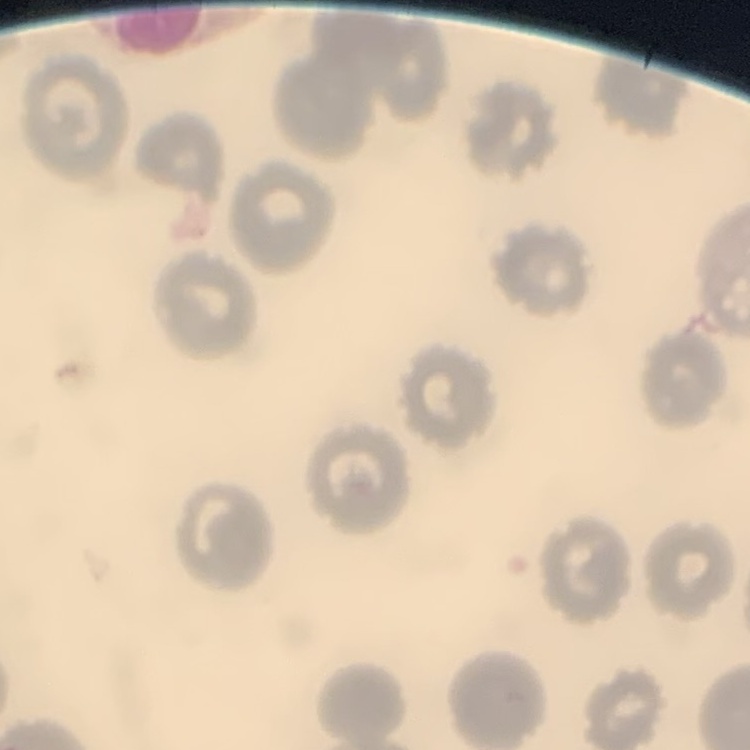

Summary:
  - Red blood cell morphology: no rouleaux formation
  - Stain: Field's or Giemsa
  - Image type: one tile cut from a larger photomicrograph
  - Preparation: thin blood smear